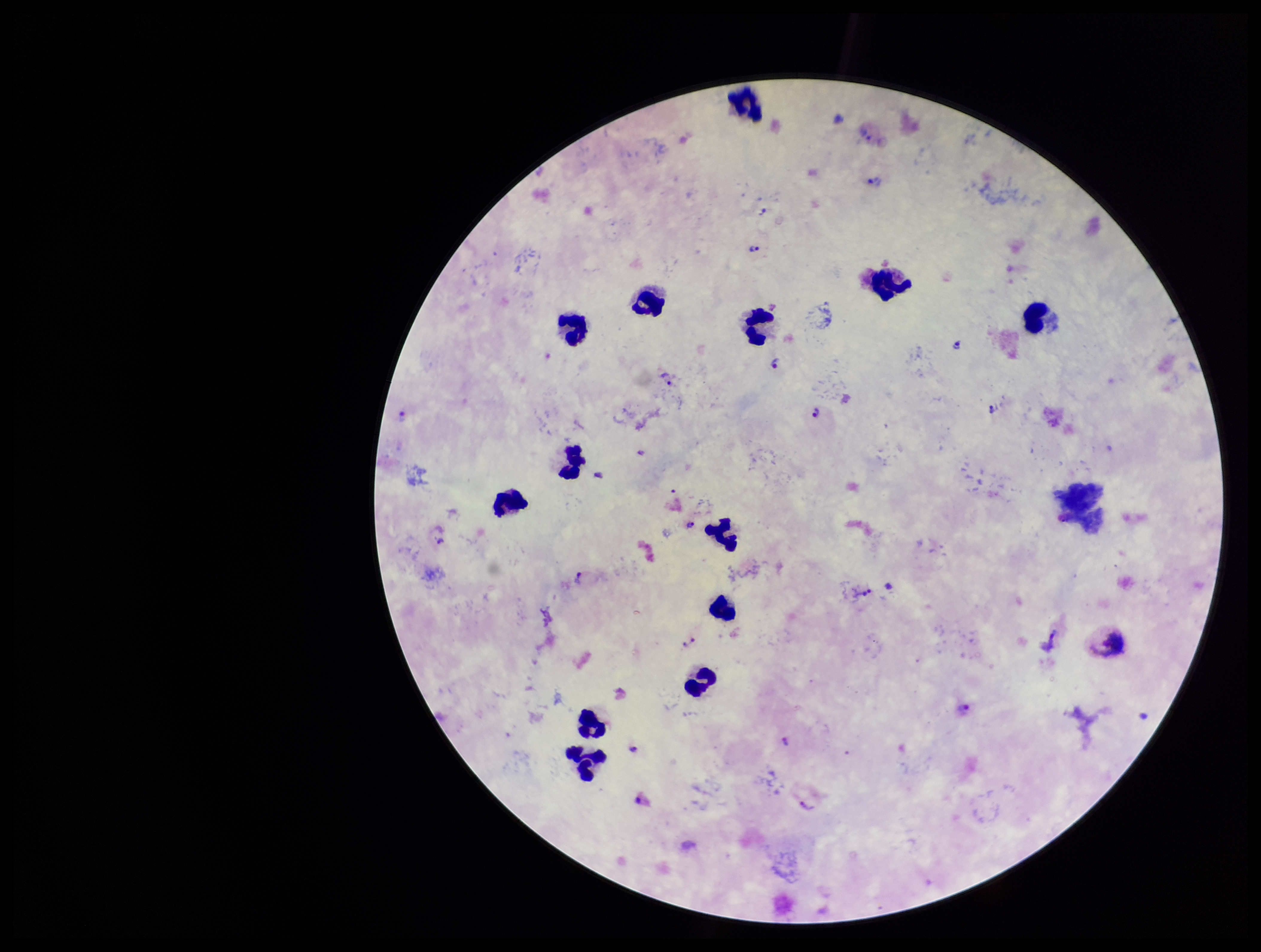

Summary:
  - Preparation: thick
  - Field of view: single
  - Stain: Giemsa
  - Leukocyte count: 13
  - Plasmodium parasites: seen
  - Parasite count: 16
  - Image size: 1261×952 pixels
  - Patient malaria status: infected
  - Capture: smartphone photograph through the microscope eyepiece
  - Species reported for this patient: Plasmodium vivax